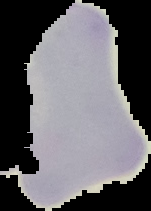 From a thin blood smear. Malaria status: uninfected. The area outside the segmented cell region is set to black. Image is 151×211 pixels.